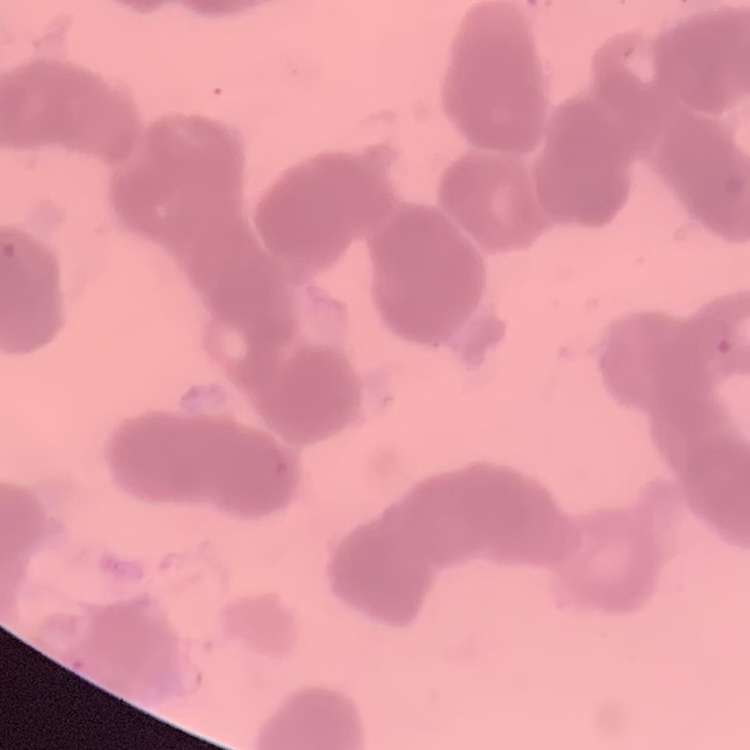

Summary:
  - Red blood cell morphology: rouleaux formation
  - Stain: Field's or Giemsa
  - Image type: square crop of a larger photomicrograph
  - Preparation: thin blood smear